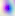

400x magnification. Toxoplasma gondii is seen. Photomicrograph.